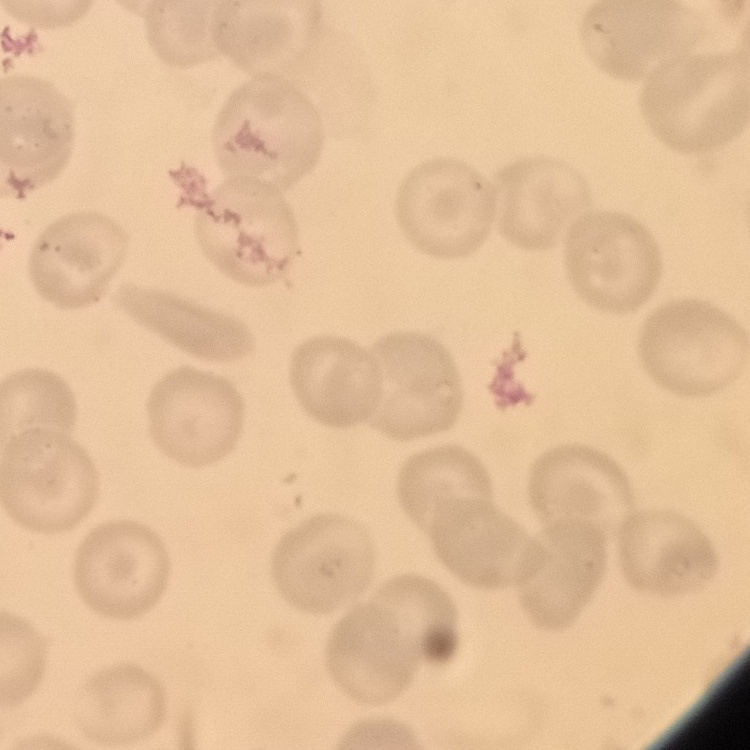
erythrocyte morphology = no rouleaux formation
image type = square crop of a larger photomicrograph
preparation = thin blood film
stain = Field's or Giemsa